Report the malaria status of this cell.
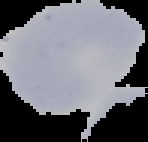
Uninfected.

Summary:
  - Image type: segmented cell region on a black background
  - Preparation: thin blood film
  - Image size: 148×142 pixels